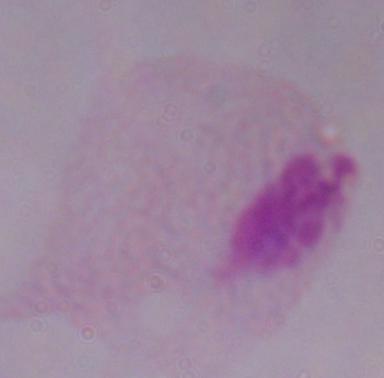

{
  "magnification": "1000x",
  "modality": "micrograph",
  "identification": "trichomonad"
}